Name the blood parasite species.
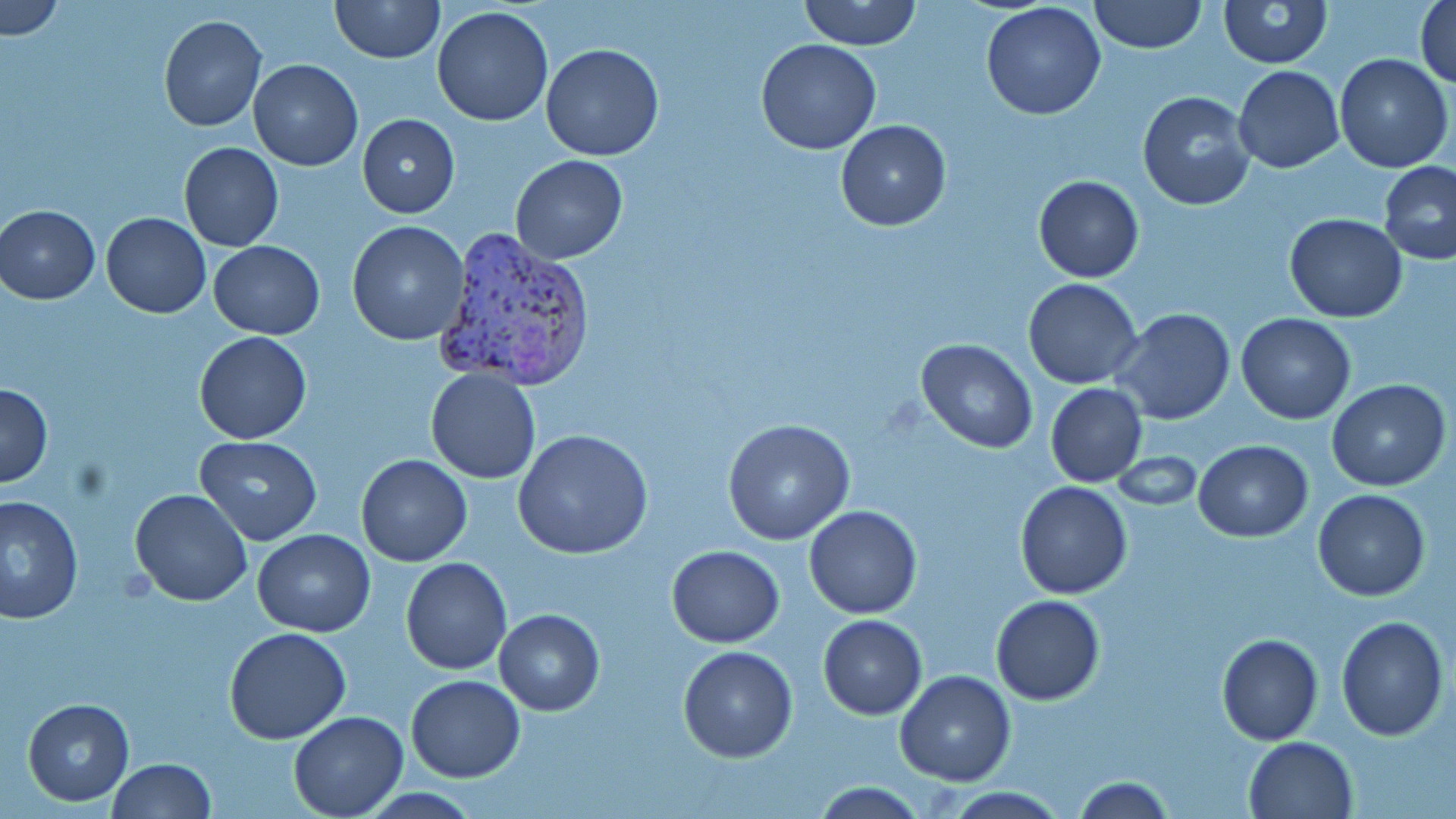
Plasmodium vivax.

magnification = 1000x
uninfected red blood cell locations = approximate bounding boxes as (x1, y1, x2, y2) in pixels: (1, 0, 65, 40), (330, 0, 444, 65), (799, 0, 921, 50), (1087, 0, 1208, 54), (1415, 0, 1456, 89), (1219, 1, 1331, 68), (981, 2, 1107, 120), (431, 6, 556, 128), (157, 14, 266, 132), (755, 38, 883, 154), (540, 42, 665, 162), (1333, 54, 1453, 173), (248, 59, 362, 170), (1233, 65, 1343, 173), (1137, 91, 1254, 211), (356, 113, 459, 220), (835, 120, 951, 232), (179, 142, 284, 252), (511, 154, 627, 265), (1378, 161, 1456, 266), (1033, 176, 1144, 283), (1, 204, 100, 304), (101, 212, 211, 319), (1284, 213, 1408, 322), (347, 220, 471, 345), (208, 240, 325, 339), (1023, 277, 1143, 388), (1112, 308, 1236, 425), (1236, 313, 1358, 424), (193, 331, 312, 444), (915, 339, 1039, 454), (425, 368, 541, 483), (1326, 380, 1451, 492), (0, 382, 52, 488), (1045, 383, 1148, 487), (722, 419, 855, 544), (513, 429, 654, 560), (194, 435, 323, 547), (1194, 440, 1313, 541), (1110, 452, 1205, 512), (357, 454, 472, 567), (1014, 482, 1135, 600), (129, 488, 253, 606), (1313, 489, 1431, 601), (1, 493, 82, 622), (804, 504, 922, 619), (252, 529, 376, 636), (665, 545, 785, 648), (401, 556, 512, 675), (992, 595, 1105, 704), (495, 608, 604, 714), (818, 614, 927, 720), (1336, 616, 1448, 740), (224, 628, 352, 744), (1217, 634, 1324, 745), (679, 646, 798, 764), (895, 670, 1016, 786), (407, 674, 525, 783), (22, 698, 134, 805), (289, 712, 409, 818), (1244, 736, 1359, 819), (105, 758, 215, 819), (1069, 776, 1176, 817), (805, 782, 932, 817), (935, 786, 1071, 818)
preparation = thin blood smear
image size = 1456×819 pixels
Plasmodium vivax-infected red blood cell locations = approximate bounding boxes as (x1, y1, x2, y2) in pixels: (432, 227, 597, 394)
stain = May-Grünwald-Giemsa
field of view = one of a larger specimen
modality = light microscopy